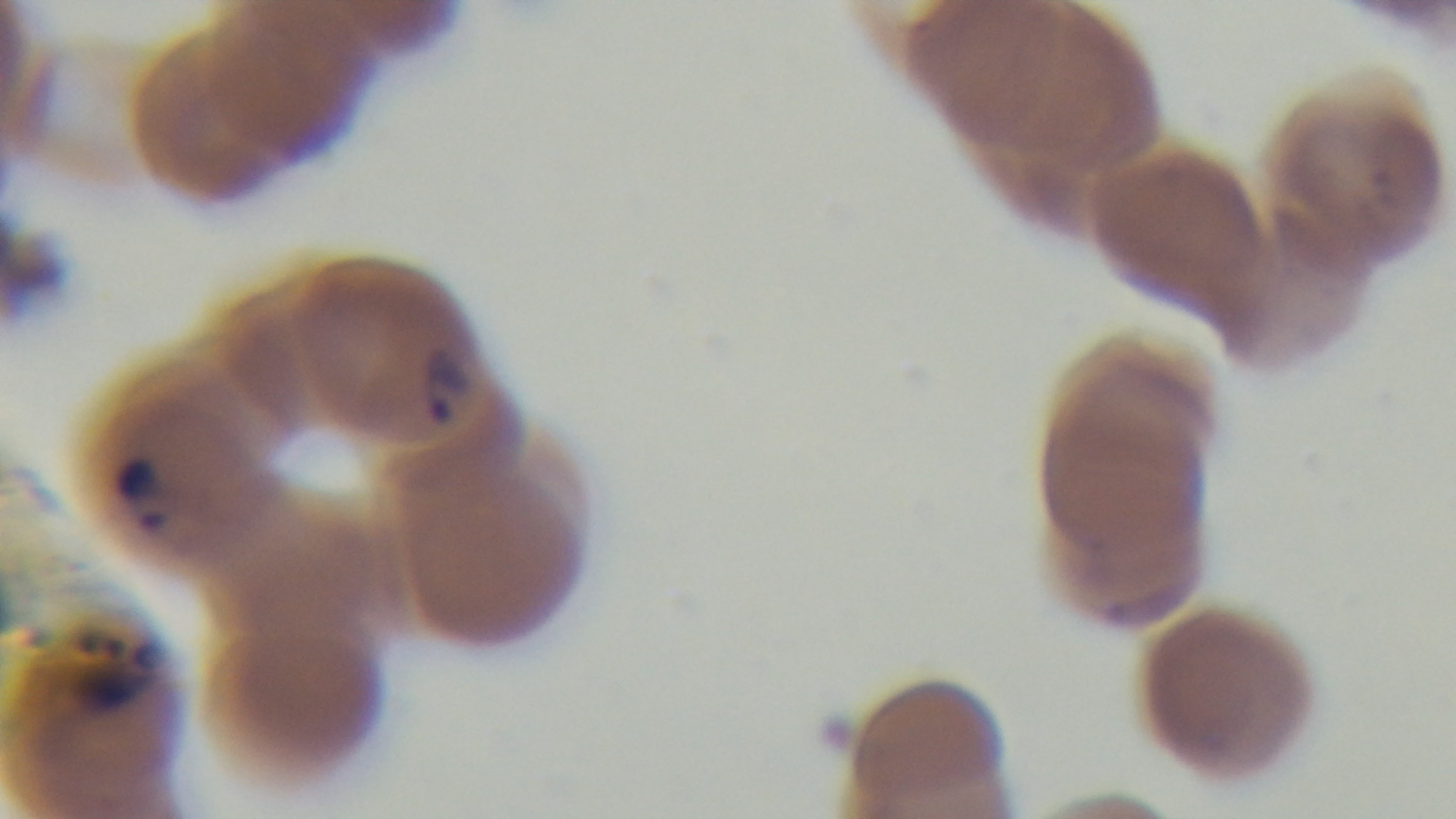

Captured with a mounted 4K digital camera. Oil-immersion objective, 100x. Malaria status: positive. One field from the slide. Giemsa-stained. Light microscopy. Preparation: thin blood film.